Mark where leukocytes are.
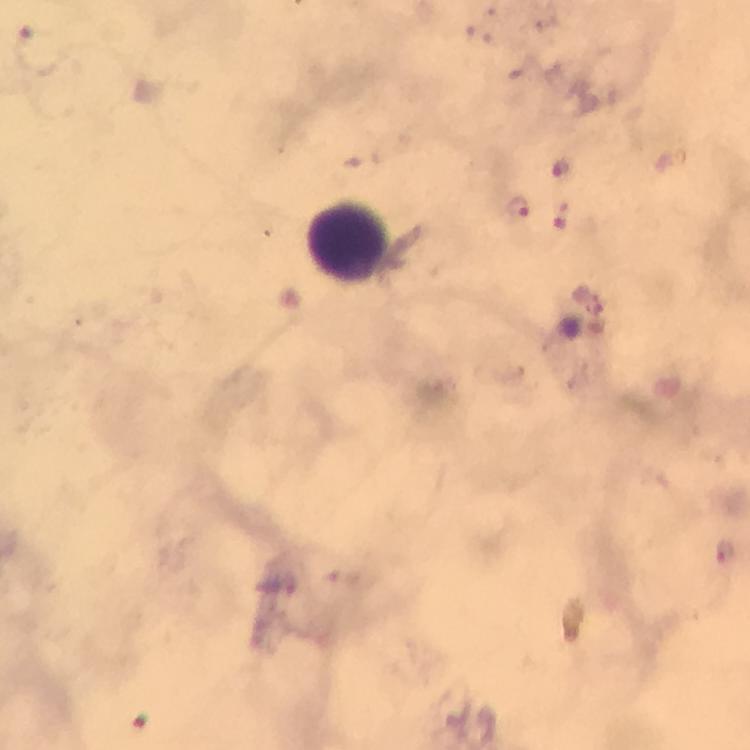

Approximate centers as {x, y} in pixels.
Leukocytes: {348, 244}.

Malaria parasite locations: {561, 169}, {517, 205}, {562, 214}, {725, 551}. Giemsa-stained preparation. Smartphone photograph taken through a microscope. Image is 750×750 pixels. Immersion oil was used. A crop from one field of view. From a diagnostic examination for malaria. 100x magnification. Thick blood film.